Name the blood parasite species.
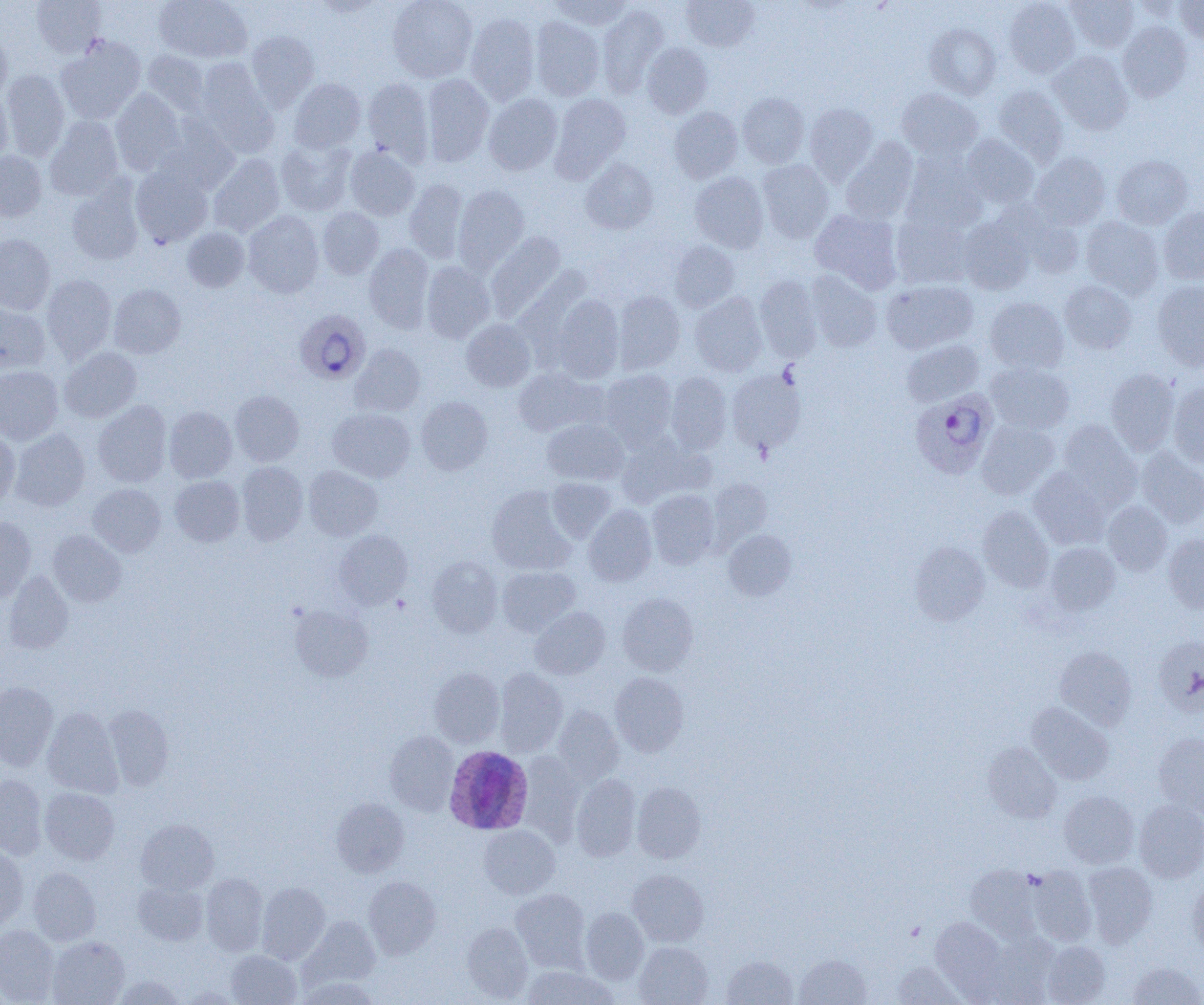

Plasmodium ovale.

field of view = single
platelet locations = approximate bounding boxes as (x1, y1, x2, y2) in pixels: (392, 596, 410, 613)
modality = optical microscopy
Plasmodium ovale-infected red blood cell locations = approximate bounding boxes as (x1, y1, x2, y2) in pixels: (294, 309, 371, 384), (910, 390, 998, 480), (444, 745, 534, 835)
preparation = thin blood smear
magnification = 1000x
image size = 1204×1005 pixels
uninfected red blood cell locations = approximate bounding boxes as (x1, y1, x2, y2) in pixels: (31, 0, 107, 59), (153, 0, 253, 64), (310, 0, 386, 17), (387, 0, 477, 82), (549, 0, 632, 30), (1004, 0, 1079, 78), (682, 1, 758, 51), (1066, 1, 1138, 52), (1175, 1, 1204, 43), (598, 5, 668, 95), (466, 13, 540, 104), (530, 17, 604, 101), (1118, 21, 1191, 102), (925, 23, 1000, 98), (245, 30, 320, 110), (0, 33, 12, 101), (55, 38, 146, 124), (642, 43, 712, 118), (141, 50, 210, 116), (1049, 51, 1133, 134), (194, 61, 279, 157), (2, 70, 70, 160), (421, 74, 494, 166), (362, 77, 434, 165), (289, 78, 365, 154), (992, 84, 1068, 164), (110, 89, 187, 176), (897, 89, 982, 159), (0, 90, 13, 166), (549, 92, 631, 180), (738, 92, 809, 168), (484, 94, 562, 175), (805, 104, 878, 184), (669, 107, 743, 183), (45, 115, 124, 200), (157, 117, 240, 195), (961, 135, 1039, 207), (275, 138, 357, 216), (841, 138, 919, 224), (344, 146, 420, 220), (0, 150, 47, 221), (902, 150, 987, 233), (1030, 152, 1110, 229), (208, 154, 285, 237), (1112, 155, 1193, 229), (580, 158, 658, 234), (757, 159, 833, 242), (131, 164, 213, 247), (690, 172, 769, 253), (66, 179, 144, 266), (404, 179, 468, 263), (452, 185, 529, 273), (1003, 202, 1084, 278), (317, 207, 384, 279), (1158, 208, 1204, 284), (810, 209, 903, 293), (243, 210, 324, 298), (892, 214, 970, 289), (1081, 217, 1164, 299), (958, 218, 1034, 294), (182, 227, 250, 292), (486, 232, 566, 321), (0, 234, 55, 315), (670, 240, 740, 312), (364, 243, 433, 333), (421, 261, 495, 343), (805, 271, 882, 352), (42, 274, 116, 363), (755, 275, 822, 361), (881, 280, 978, 353), (1059, 280, 1137, 354), (1152, 281, 1204, 370), (108, 284, 186, 358), (613, 291, 685, 374), (690, 292, 767, 376), (551, 294, 624, 382), (985, 297, 1069, 374), (0, 302, 50, 377), (461, 319, 536, 391), (902, 340, 983, 406), (350, 344, 425, 416), (59, 347, 142, 422), (986, 362, 1075, 434), (0, 365, 63, 444), (512, 367, 606, 437), (726, 367, 806, 455), (1105, 368, 1179, 454), (600, 369, 677, 448), (666, 372, 732, 454), (1169, 382, 1204, 467), (230, 390, 304, 467), (416, 396, 492, 475), (93, 401, 172, 487), (164, 406, 237, 482), (328, 408, 415, 482), (542, 419, 628, 485), (977, 420, 1060, 499), (1058, 420, 1141, 507), (10, 428, 90, 511), (0, 430, 19, 508), (616, 434, 704, 508), (1136, 448, 1204, 528), (236, 462, 308, 545), (304, 465, 383, 541), (1028, 467, 1110, 549), (169, 475, 244, 546), (546, 478, 616, 542), (710, 478, 771, 544), (88, 483, 166, 557), (487, 485, 576, 574), (647, 490, 720, 569), (1102, 501, 1172, 576), (583, 504, 657, 586), (978, 505, 1054, 592), (0, 517, 36, 602), (334, 529, 413, 609), (724, 529, 796, 600), (48, 530, 126, 606), (1163, 535, 1204, 613), (909, 542, 989, 625), (1045, 542, 1120, 615), (427, 556, 503, 638), (497, 566, 580, 636), (3, 570, 73, 654), (617, 593, 698, 675), (290, 604, 373, 681), (530, 606, 610, 679), (1153, 637, 1204, 718), (1054, 646, 1136, 729), (429, 667, 504, 746), (494, 668, 567, 755), (610, 672, 689, 756), (0, 682, 58, 770), (1027, 702, 1113, 785), (103, 705, 173, 790), (552, 706, 623, 784), (43, 707, 122, 797), (384, 731, 459, 815), (1153, 732, 1204, 815), (983, 742, 1061, 823), (518, 752, 583, 843), (571, 774, 640, 861), (0, 775, 47, 860), (632, 782, 706, 863), (40, 787, 120, 864), (1058, 791, 1139, 868), (331, 798, 409, 877), (1135, 800, 1204, 883), (136, 819, 219, 894), (479, 825, 559, 898), (0, 845, 28, 930), (1082, 862, 1157, 946), (966, 865, 1042, 941), (1028, 866, 1097, 947), (28, 867, 101, 944), (628, 869, 709, 946), (201, 873, 268, 956), (364, 876, 441, 958), (1187, 877, 1204, 958), (132, 881, 208, 945), (257, 882, 330, 964), (511, 889, 590, 970), (580, 908, 649, 984), (300, 916, 380, 989), (930, 918, 1007, 997), (462, 922, 533, 1002), (0, 925, 60, 1004), (48, 936, 129, 1005), (969, 938, 1056, 1005), (1042, 940, 1110, 1005), (634, 941, 713, 1005), (226, 950, 301, 1005), (794, 954, 872, 1005), (722, 955, 798, 1004), (892, 961, 967, 1005), (1128, 962, 1203, 1005), (521, 965, 617, 1005), (113, 975, 185, 1004), (296, 975, 381, 1005), (179, 986, 243, 1004)